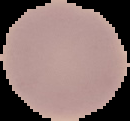

image_size: 130×121 pixels
malaria_status: uninfected
image_type: segmented cell region on a black background
preparation: thin blood smear